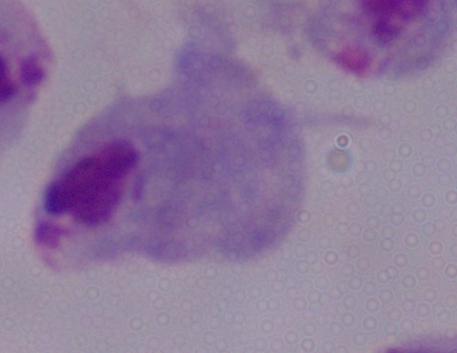

Summary:
  - Magnification: 1000x
  - Identification: trichomonad
  - Modality: photomicrograph